Locate the red blood cells and classify each one as Plasmodium falciparum-infected, uninfected, or of indeterminate infection status.
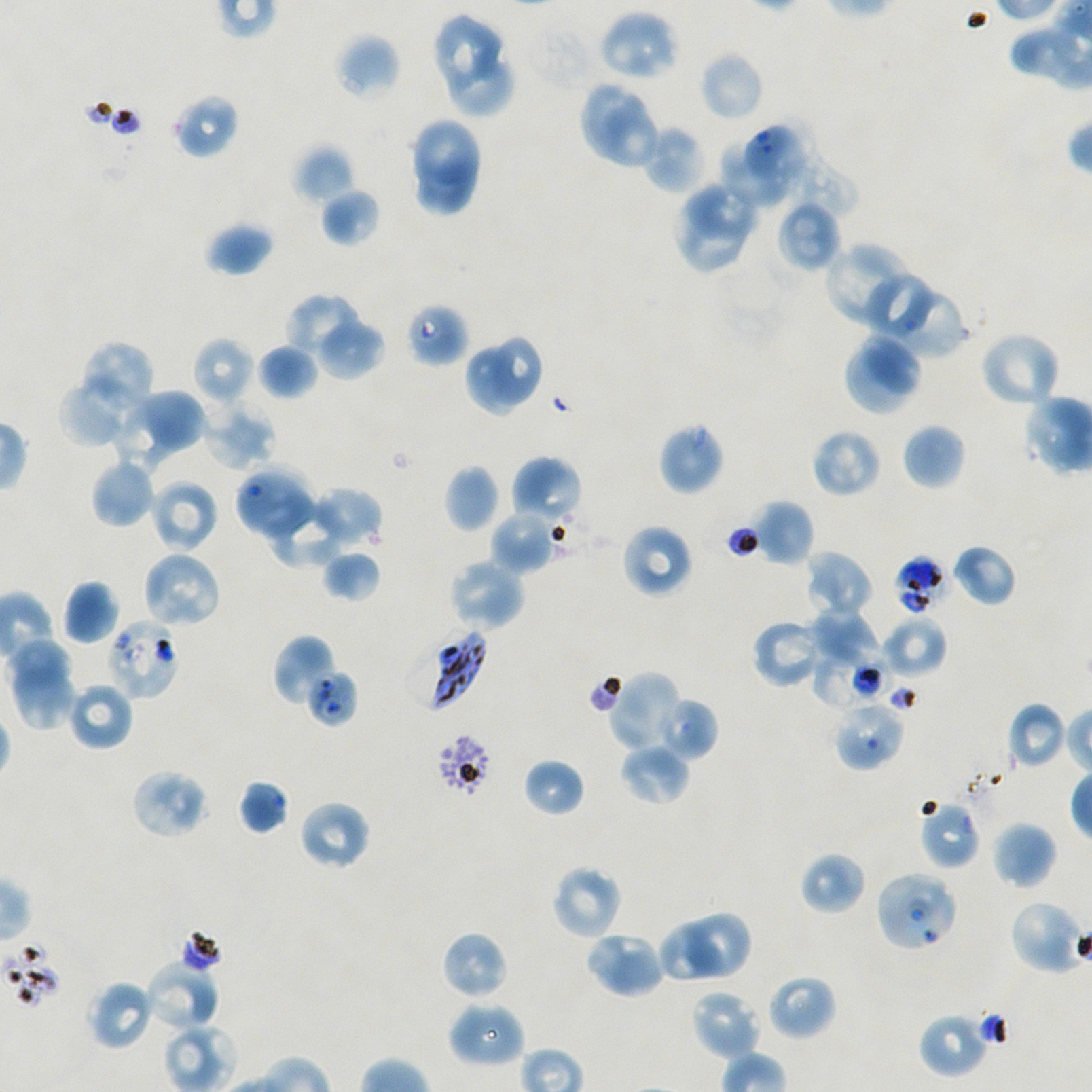
Approximate bounding boxes as (x1, y1, x2, y2) in pixels. Not every red blood cell is marked.
Infected red blood cells: (406, 623, 488, 713).
Red blood cells of indeterminate infection status: (405, 302, 469, 367), (894, 554, 947, 615), (107, 618, 180, 702), (810, 656, 896, 706), (306, 669, 358, 727), (917, 799, 981, 871), (874, 870, 958, 952).
Uninfected red blood cells: (597, 9, 680, 82), (431, 12, 507, 101), (336, 33, 401, 101), (699, 50, 765, 122), (445, 55, 514, 118), (578, 81, 645, 160), (172, 94, 239, 159), (597, 103, 660, 165), (412, 117, 484, 185), (641, 124, 705, 194), (746, 125, 801, 185), (760, 128, 858, 219), (721, 139, 794, 209), (293, 145, 355, 204), (414, 151, 479, 213), (687, 181, 757, 242), (318, 187, 380, 247), (774, 202, 837, 271), (679, 206, 744, 271), (204, 222, 274, 276), (824, 242, 907, 323), (867, 276, 933, 335), (285, 293, 363, 361), (892, 295, 966, 354), (316, 318, 385, 378), (979, 330, 1062, 410), (856, 333, 923, 392), (492, 335, 542, 404), (192, 337, 255, 407), (81, 342, 156, 414), (255, 343, 318, 401), (843, 346, 911, 416), (463, 349, 524, 416), (57, 376, 138, 448), (133, 388, 207, 450), (201, 402, 276, 471), (110, 404, 179, 471), (657, 422, 725, 496), (902, 422, 966, 490), (810, 428, 882, 499), (510, 455, 583, 527), (90, 457, 158, 528), (444, 464, 500, 532), (234, 466, 317, 543), (149, 478, 219, 553), (310, 487, 383, 549), (267, 496, 346, 568), (752, 499, 814, 566), (490, 510, 561, 575), (621, 524, 694, 598), (951, 544, 1017, 607), (321, 550, 381, 603), (804, 550, 873, 619), (141, 551, 222, 631), (447, 558, 527, 632), (62, 579, 120, 645), (807, 609, 879, 666), (880, 615, 947, 680), (751, 619, 826, 689), (272, 635, 337, 706), (7, 638, 73, 693), (12, 662, 77, 731), (606, 671, 683, 754), (66, 680, 134, 751), (657, 696, 718, 761), (832, 699, 905, 771), (1005, 702, 1068, 770), (619, 742, 691, 806), (523, 758, 585, 817), (131, 769, 208, 839), (237, 778, 290, 835), (298, 800, 372, 871), (990, 820, 1057, 890), (799, 852, 867, 915), (550, 864, 623, 941), (1007, 899, 1085, 975), (688, 913, 751, 975), (659, 924, 722, 983), (441, 930, 509, 1000), (583, 930, 667, 999), (144, 960, 220, 1031), (765, 972, 837, 1041), (87, 979, 157, 1050), (689, 988, 761, 1061), (448, 1000, 526, 1070), (917, 1012, 989, 1078).

preparation = thin blood smear
stain = Giemsa
objective = 100x, oil immersion, numerical aperture 1.45
field of view = one from this slide
image size = 1092×1092 pixels
donor blood group = A+/O+
culture = in-vitro Plasmodium falciparum strain NF54, static